Assess the morphology of the red blood cells.
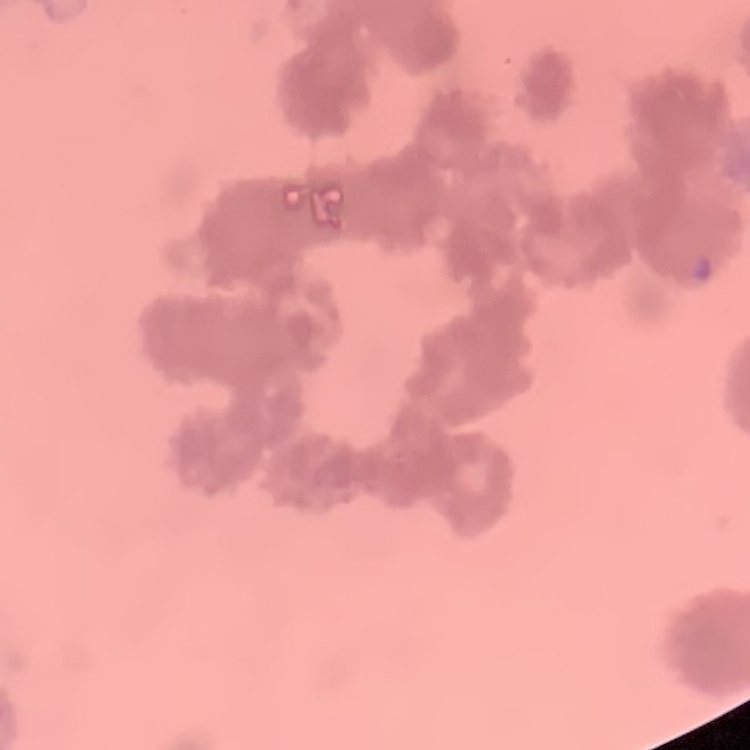

They show rouleaux formation.

Thin peripheral smear. Stained with either Field's or Giemsa. Square crop of a larger photomicrograph.